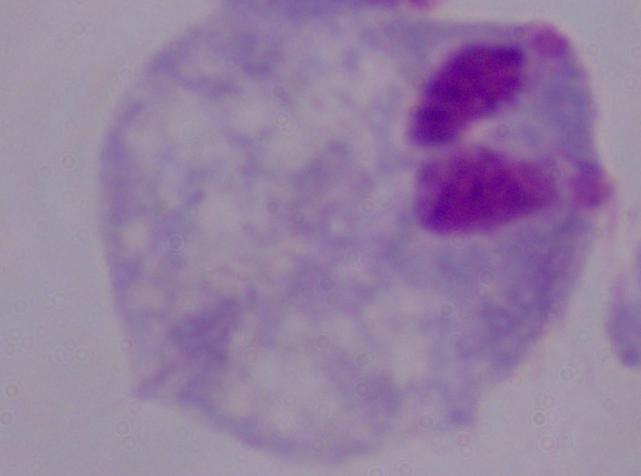
A trichomonad is shown. Photomicrograph. Captured at 1000x magnification.